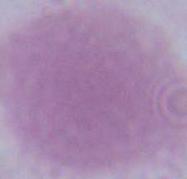
Summary:
  - Magnification: 1000x
  - Modality: micrograph
  - Identification: red blood cell